Assess the morphology of the red blood cells.
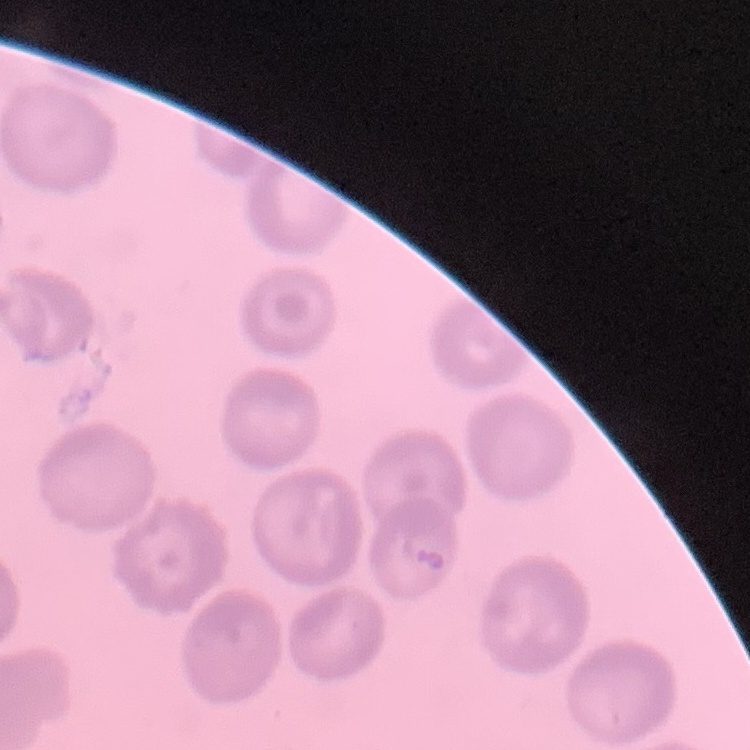

No rouleaux formation.

Summary:
  - Image type: one tile cut from a larger photomicrograph
  - Stain: Field's or Giemsa
  - Preparation: thin blood film